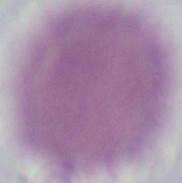

Summary:
  - Identification: red blood cell
  - Modality: micrograph
  - Magnification: 1000x